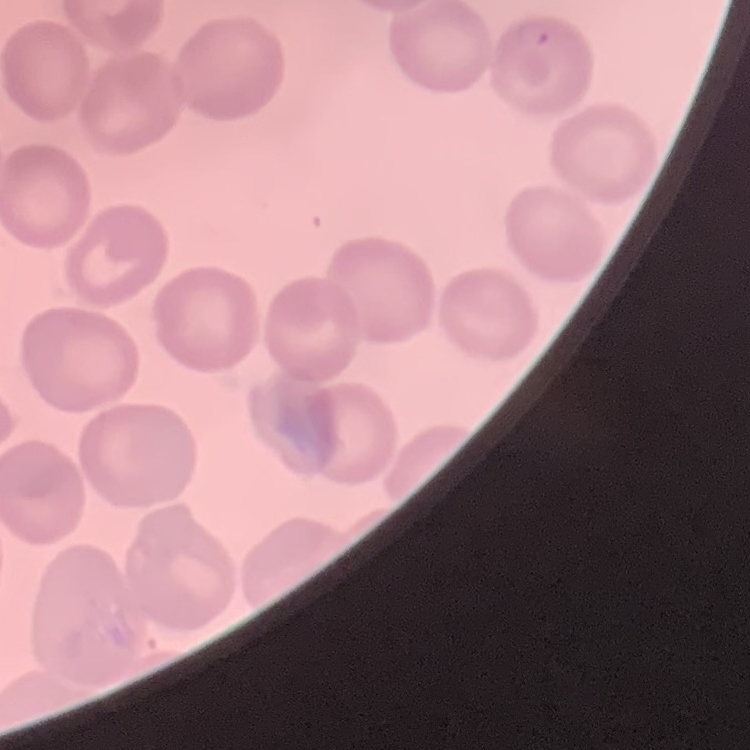 The red blood cells exhibit no rouleaux formation. Thin blood smear. Stained with either Field's or Giemsa. Square crop of a larger photomicrograph.